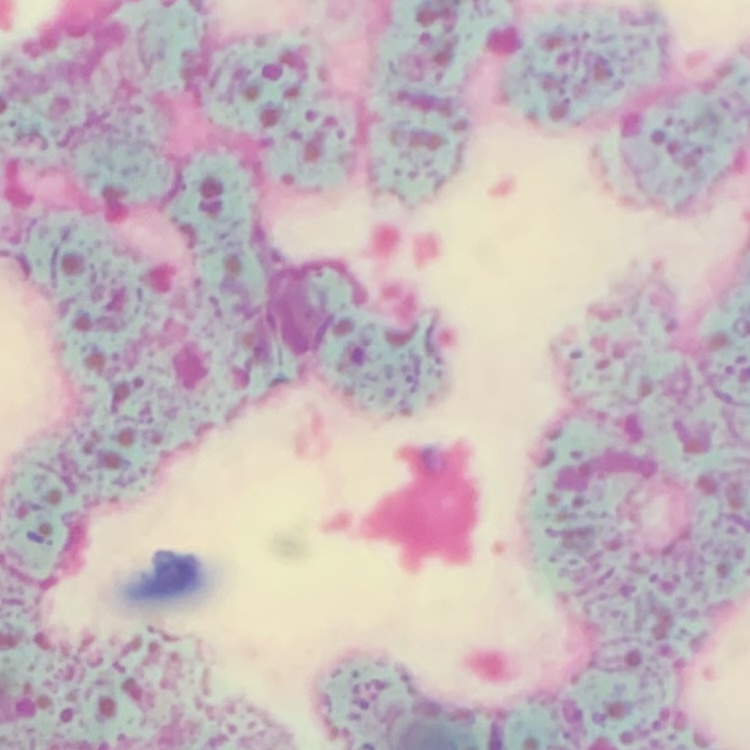
red blood cell morphology = rouleaux formation
preparation = thin blood smear
image type = square crop of a larger photomicrograph
stain = Field's or Giemsa